Locate every blood parasite and identify its species.
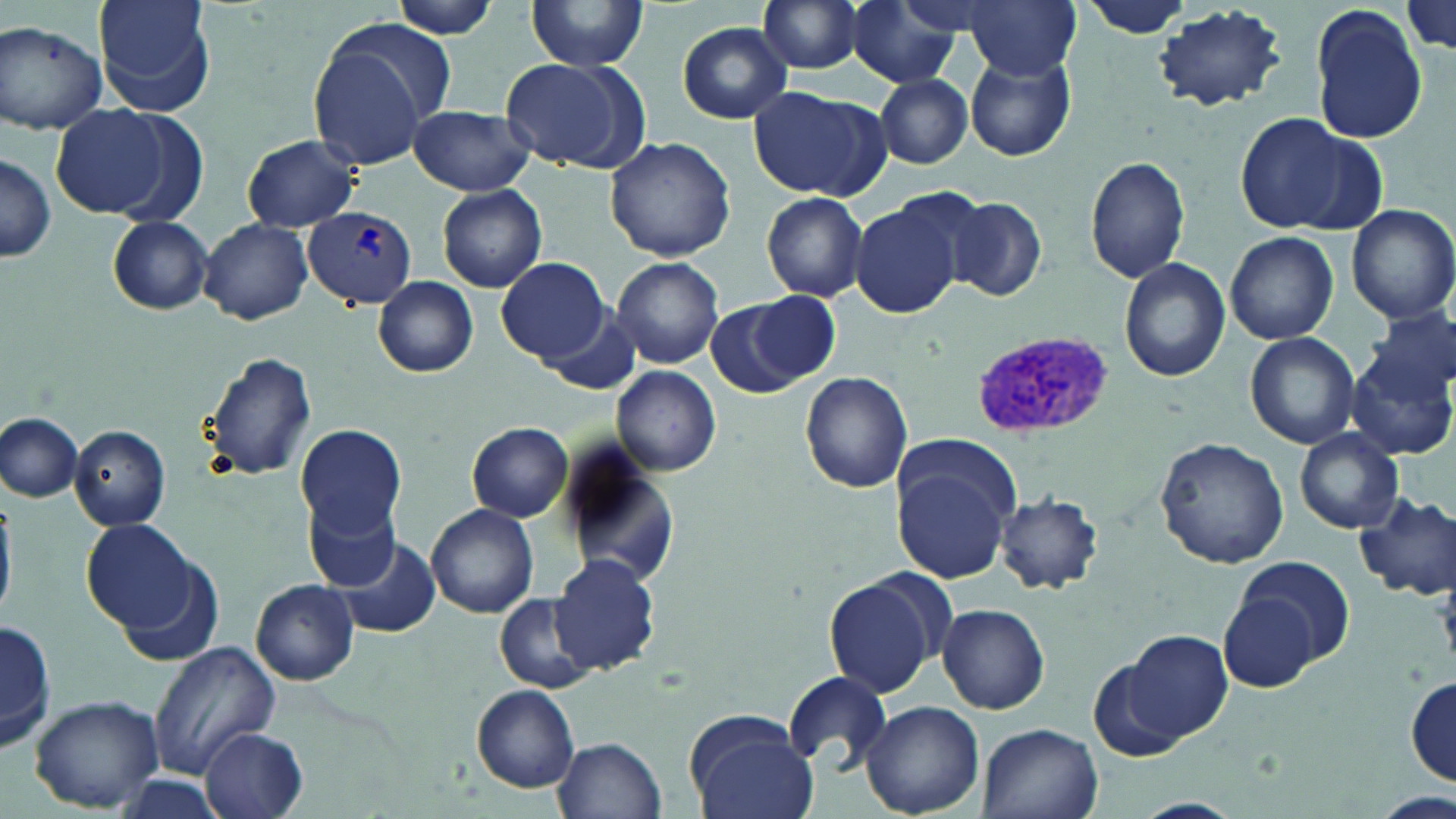
Approximate bounding boxes as (x1,y1)-(x2,y2) corner pairs in pixels.
Plasmodium vivax-infected red blood cells: (302,207)-(416,308), (973,330)-(1118,439).
No Plasmodium falciparum, Plasmodium ovale, Plasmodium malariae, Babesia divergens, or Trypanosoma brucei observed.

Summary:
  - Uninfected red blood cell locations: (94,0)-(218,115), (392,0)-(503,39), (526,0)-(650,71), (757,0)-(871,74), (845,0)-(964,87), (963,0)-(1080,79), (1082,1)-(1191,42), (1400,1)-(1456,52), (1154,4)-(1287,109), (1313,7)-(1428,143), (1,20)-(107,134), (678,21)-(793,124), (308,24)-(448,172), (965,52)-(1076,161), (499,58)-(646,173), (875,74)-(973,168), (749,84)-(890,200), (49,103)-(173,217), (408,103)-(535,196), (1232,111)-(1376,236), (241,134)-(362,232), (604,137)-(736,262), (1,150)-(57,265), (1085,154)-(1191,284), (434,184)-(548,292), (761,192)-(869,303), (947,195)-(1047,302), (849,200)-(967,318), (1348,204)-(1456,326), (106,217)-(214,313), (200,218)-(313,323), (1225,231)-(1338,346), (612,255)-(725,369), (497,256)-(611,365), (1119,258)-(1231,381), (374,277)-(478,376), (747,293)-(843,386), (705,297)-(809,399), (538,301)-(644,393), (1366,309)-(1455,401), (1245,332)-(1359,448), (201,347)-(320,482), (1347,350)-(1455,462), (613,366)-(722,475), (799,372)-(913,495), (0,411)-(82,502), (466,421)-(573,522), (296,423)-(407,538), (70,425)-(170,529), (1295,429)-(1404,533), (1155,437)-(1289,569), (556,445)-(681,590), (894,462)-(1013,583), (303,491)-(400,593), (997,491)-(1105,594), (1353,491)-(1456,598), (0,492)-(22,622), (426,503)-(540,619), (82,520)-(197,633), (335,536)-(441,638), (109,541)-(225,666), (550,553)-(661,677), (1236,554)-(1354,670), (823,570)-(950,699), (251,579)-(359,685), (496,595)-(594,692), (1218,595)-(1319,691), (936,604)-(1049,714), (0,615)-(53,756), (1125,631)-(1231,740), (146,640)-(282,779), (1088,659)-(1190,763), (784,671)-(892,774), (1407,675)-(1455,785), (472,685)-(580,793), (28,694)-(164,812), (859,700)-(984,819), (688,717)-(822,819), (976,723)-(1103,819), (200,728)-(306,819), (556,735)-(666,818)
  - Slide-level diagnosis: Plasmodium vivax
  - Stain: May-Grünwald-Giemsa
  - Field of view: single
  - Magnification: 1000x
  - Modality: optical microscopy
  - Preparation: thin blood film
  - Image size: 1456×819 pixels